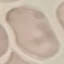

{
  "malaria_status": "uninfected",
  "preparation": "thin blood film",
  "stain": "Giemsa",
  "capture": "smartphone through the microscope eyepiece",
  "image_type": "cell patch, automatically extracted from a larger field of view and resized to 64 × 64 pixels"
}